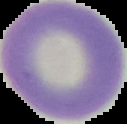
malaria_status: uninfected
image_size: 127×124 pixels
preparation: thin blood smear
image_type: segmented cell region on a black background